Report the malaria status of this cell.
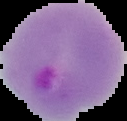
Parasitized.

The area outside the segmented cell region is set to black. Image is 127×121 pixels. From a thin blood smear.